Report the malaria status of this cell.
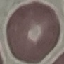
It is uninfected.

{
  "image_type": "automatically extracted cell patch, resized to 64 × 64 pixels",
  "capture": "smartphone camera at the microscope eyepiece",
  "stain": "Giemsa",
  "preparation": "thin blood film"
}